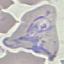 Result: malaria parasites identified. Automatically extracted cell patch, resized to 64 × 64 pixels. Thin blood smear. Acquired by smartphone through the microscope eyepiece. Giemsa-stained preparation.